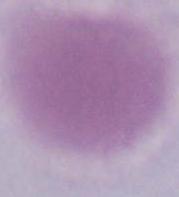
{
  "modality": "micrograph",
  "identification": "red blood cell",
  "magnification": "1000x"
}